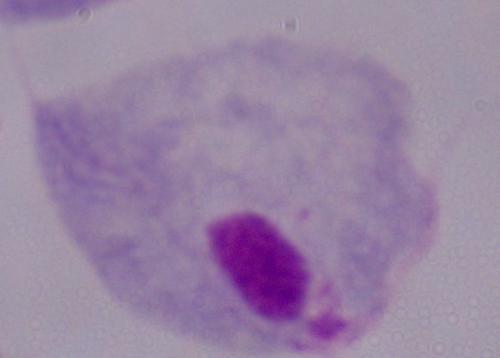

{
  "magnification": "1000x",
  "identification": "trichomonad",
  "modality": "photomicrograph"
}